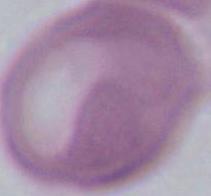
Summary:
  - Modality: photomicrograph
  - Magnification: 1000x
  - Identification: erythrocyte